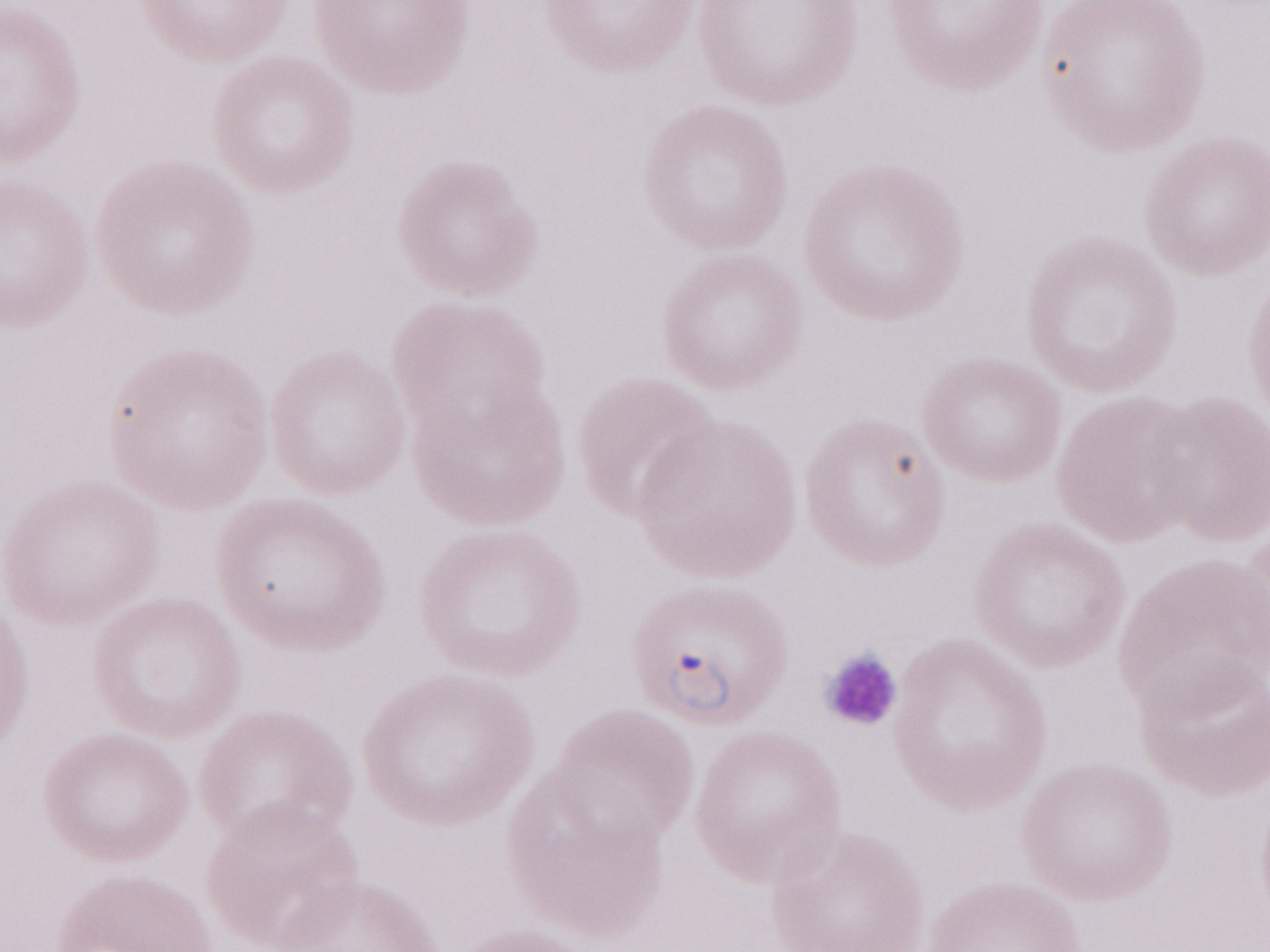
Thin blood smear. May-Grünwald-Giemsa (MGG) stain. Single field of view. Image is 1270×952 pixels. Olympus BX43 microscope, Olympus DP73 camera. Patient diagnosis: malaria infection. 1,000x magnification.